Describe the morphology of the erythrocytes.
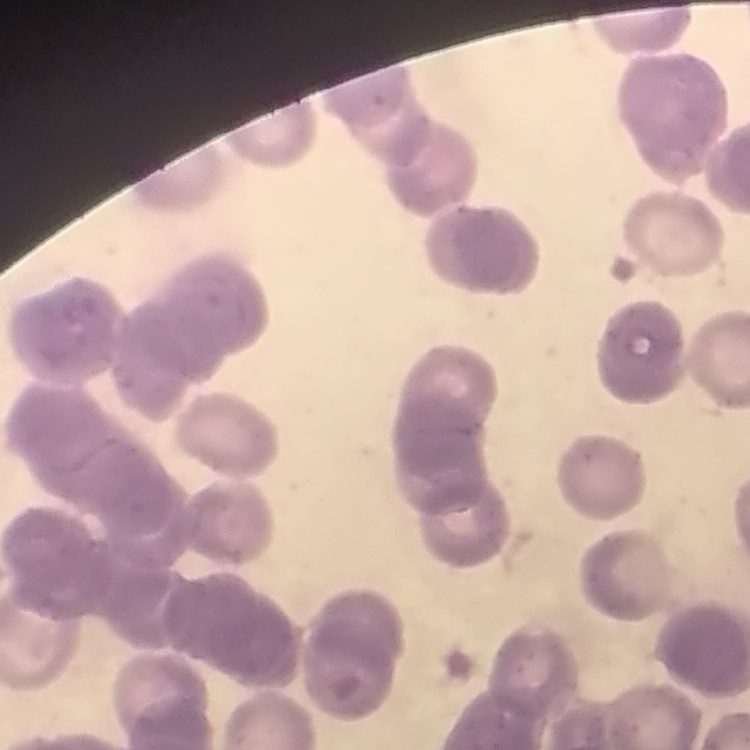

Rouleaux formation.

Square crop of a larger photomicrograph. Thin blood smear. Stained with either Field's or Giemsa.